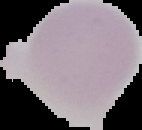

image_type: segmented cell region with the area outside set to black
image_size: 142×130 pixels
malaria_status: uninfected
preparation: thin blood smear